Locate and identify every blood parasite.
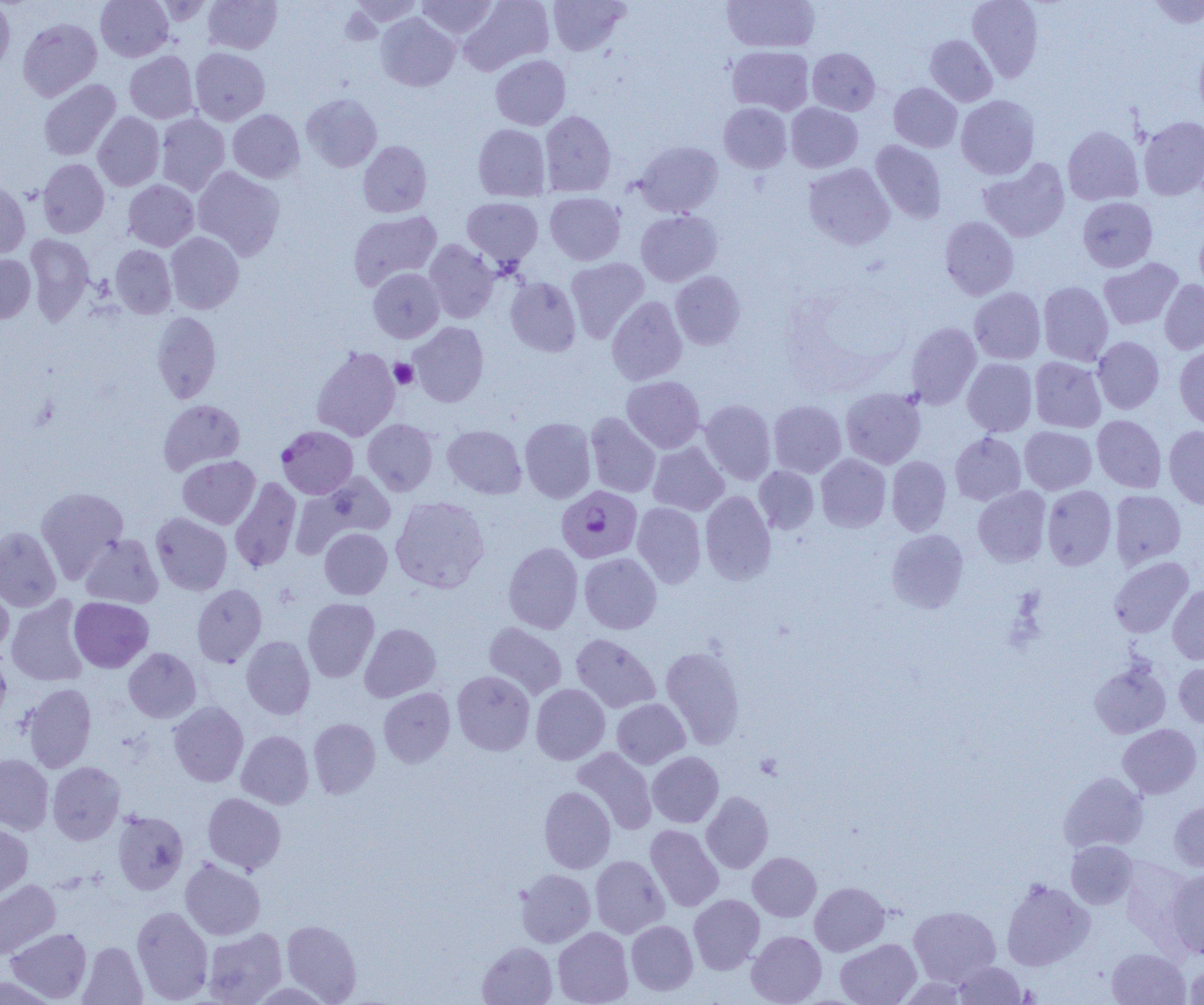

Approximate bounding boxes as (x1,y1)-(x2,y2) corner pairs in pixels.
Plasmodium falciparum-infected red blood cells: (277,426)-(358,499), (556,485)-(642,563).
No Plasmodium ovale, Plasmodium malariae, Plasmodium vivax, Babesia divergens, or Trypanosoma brucei observed.

Summary:
  - Platelet locations: (389,359)-(418,388)
  - Uninfected red blood cell locations: (95,0)-(173,61), (203,0)-(281,54), (345,0)-(424,30), (417,0)-(498,39), (459,0)-(554,75), (548,0)-(630,55), (722,0)-(820,53), (967,0)-(1043,82), (1146,0)-(1203,28), (0,1)-(15,74), (376,13)-(459,91), (18,18)-(102,101), (925,34)-(997,106), (1194,39)-(1204,123), (727,46)-(814,115), (190,47)-(270,125), (808,48)-(880,115), (125,51)-(198,123), (490,55)-(570,130), (38,79)-(121,161), (889,82)-(962,152), (301,93)-(382,172), (956,95)-(1039,180), (719,102)-(791,173), (786,103)-(862,173), (228,109)-(305,183), (539,110)-(616,197), (93,112)-(164,191), (156,113)-(230,195), (1138,116)-(1204,200), (473,124)-(550,201), (1063,125)-(1143,206), (358,140)-(432,217), (870,140)-(947,224), (634,141)-(723,217), (37,158)-(109,238), (979,158)-(1070,243), (804,163)-(895,250), (193,166)-(285,260), (0,180)-(30,258), (123,180)-(198,251), (545,192)-(625,265), (462,197)-(543,267), (1078,197)-(1157,272), (348,210)-(442,290), (636,210)-(722,286), (940,216)-(1018,300), (1194,221)-(1204,299), (165,232)-(244,314), (25,234)-(94,325), (424,239)-(499,323), (110,245)-(176,318), (0,254)-(36,323), (566,257)-(649,343), (1099,258)-(1183,330), (368,268)-(444,342), (670,271)-(745,350), (505,277)-(581,356), (1159,279)-(1204,354), (1038,281)-(1113,366), (969,287)-(1046,364), (607,296)-(687,385), (152,311)-(221,404), (409,322)-(488,407), (905,322)-(981,408), (1093,336)-(1164,414), (1174,345)-(1204,431), (311,346)-(400,441), (1029,356)-(1106,433), (963,358)-(1037,436), (622,376)-(705,453), (841,388)-(926,468), (158,399)-(245,474), (700,399)-(776,485), (768,400)-(846,478), (585,412)-(661,498), (1092,415)-(1166,492), (520,418)-(596,503), (363,419)-(438,495), (442,425)-(526,499), (1164,425)-(1204,509), (1020,426)-(1096,494), (950,432)-(1026,505), (647,441)-(729,516), (816,454)-(891,532), (178,455)-(260,529), (887,456)-(951,536), (754,465)-(819,534), (302,472)-(397,547), (230,477)-(302,573), (1043,485)-(1117,570), (36,486)-(129,582), (973,486)-(1051,567), (1110,489)-(1185,569), (700,491)-(776,585), (390,496)-(490,593), (632,502)-(706,588), (151,512)-(232,595), (0,526)-(61,612), (320,528)-(392,599), (886,528)-(969,614), (80,534)-(163,608), (503,542)-(583,633), (579,552)-(661,634), (1109,556)-(1193,638), (0,580)-(13,656), (192,584)-(267,667), (1168,585)-(1204,664), (6,596)-(89,686), (69,597)-(153,672), (303,597)-(379,682), (484,622)-(567,699), (359,623)-(440,702), (571,633)-(660,713), (241,636)-(315,719), (660,645)-(746,749), (124,648)-(201,723), (0,651)-(11,723), (1089,660)-(1171,739), (1174,662)-(1204,728), (452,670)-(535,755), (22,683)-(97,772), (531,683)-(610,764), (378,688)-(455,767), (612,698)-(690,768), (169,701)-(248,787), (308,718)-(380,798), (1117,724)-(1202,799), (236,730)-(313,809), (572,747)-(657,835), (647,751)-(723,827), (0,754)-(53,834), (47,761)-(125,844), (1058,771)-(1148,853), (539,786)-(615,873), (701,791)-(773,873), (203,793)-(285,873), (1169,800)-(1204,872), (113,810)-(188,895), (0,822)-(33,900), (645,824)-(724,911), (1066,841)-(1138,909), (748,852)-(821,921), (590,855)-(669,938), (180,858)-(265,940), (1120,858)-(1194,946), (1167,868)-(1204,959), (515,869)-(595,947), (1001,878)-(1093,971), (0,879)-(60,958), (810,882)-(890,955), (688,894)-(764,973), (909,905)-(1001,986), (131,906)-(213,1003), (281,919)-(362,1003), (626,920)-(698,995), (6,927)-(92,1002), (553,927)-(633,1005), (202,928)-(287,1004), (746,930)-(826,1005), (835,938)-(921,1005), (78,941)-(147,1004), (477,942)-(558,1005), (1107,948)-(1190,1005), (953,961)-(1026,1004), (1184,963)-(1204,1004), (0,974)-(58,1005)
  - Slide-level diagnosis: Plasmodium falciparum
  - Modality: light microscopy
  - Field of view: one of a larger specimen
  - Image size: 1204×1005 pixels
  - Preparation: thin blood smear
  - Magnification: 1000x